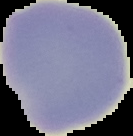

malaria status = uninfected
preparation = thin blood smear
image size = 133×136 pixels
image type = cell region segmented out of the field of view; surrounding area masked to black